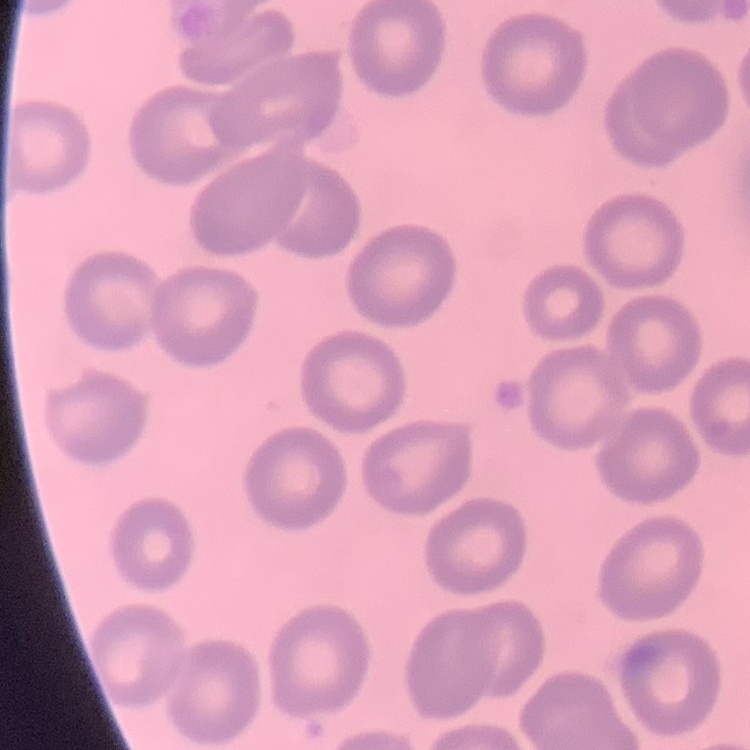

Summary:
  - Red blood cell morphology: no rouleaux formation
  - Preparation: thin blood film
  - Image type: one tile cut from a larger photomicrograph
  - Stain: Field's or Giemsa